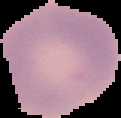
{
  "image_type": "segmented cell region with the area outside set to black",
  "image_size": "121×118 pixels",
  "preparation": "thin blood smear",
  "malaria_status": "uninfected"
}